Locate every Plasmodium falciparum-infected red blood cell.
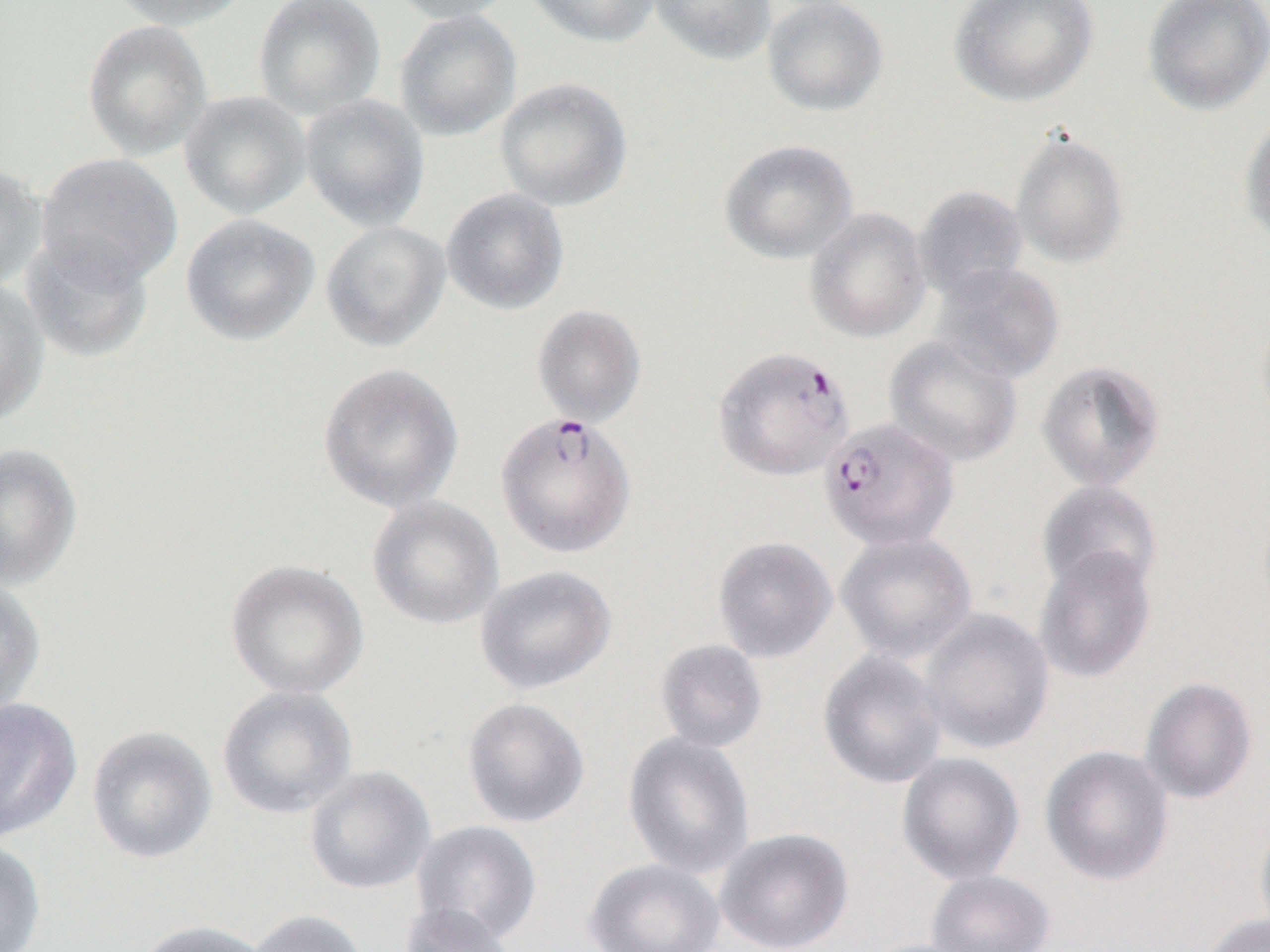
Approximate bounding boxes as [x1, y1, x2, y2] in pixels.
Plasmodium falciparum-infected red blood cells: [713, 346, 855, 482], [495, 411, 637, 558], [819, 418, 960, 552].

Uninfected red blood cell locations: [106, 0, 254, 30], [253, 0, 386, 120], [384, 0, 521, 24], [524, 0, 662, 48], [649, 0, 777, 65], [762, 0, 889, 117], [950, 0, 1099, 106], [1143, 0, 1270, 116], [393, 9, 522, 141], [81, 19, 213, 161], [495, 77, 633, 212], [179, 90, 312, 220], [299, 94, 429, 231], [1238, 113, 1270, 248], [1010, 129, 1130, 269], [719, 139, 858, 264], [35, 153, 183, 287], [0, 162, 46, 291], [913, 185, 1029, 301], [441, 188, 569, 315], [805, 207, 932, 343], [181, 213, 319, 346], [321, 221, 451, 352], [20, 233, 154, 363], [930, 262, 1064, 384], [0, 279, 49, 426], [531, 304, 647, 427], [1256, 311, 1270, 436], [884, 336, 1023, 467], [1036, 360, 1165, 491], [318, 363, 464, 514], [0, 443, 82, 590], [1037, 481, 1163, 596], [367, 496, 504, 631], [836, 531, 977, 662], [712, 535, 838, 663], [1034, 547, 1156, 683], [225, 559, 369, 700], [475, 565, 617, 695], [0, 574, 46, 718], [919, 608, 1054, 754], [654, 639, 768, 752], [818, 650, 947, 789], [1140, 677, 1258, 804], [217, 685, 357, 819], [0, 697, 82, 842], [462, 697, 590, 828], [86, 726, 218, 864], [623, 733, 755, 878], [1040, 745, 1174, 886], [897, 752, 1025, 885], [303, 765, 436, 895], [1254, 814, 1270, 940], [411, 820, 542, 947], [716, 828, 854, 952], [0, 837, 46, 952], [584, 858, 724, 952], [926, 870, 1055, 952], [399, 903, 519, 952], [245, 909, 370, 952], [1200, 913, 1270, 952], [134, 920, 273, 952]. Slide-level diagnosis: Plasmodium falciparum. Image is 1270×952 pixels. One field of a larger specimen. Thin blood smear. Captured at 1000x magnification. Light microscopy.